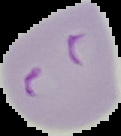

Summary:
  - Preparation: thin blood film
  - Image type: segmented cell region with the area outside set to black
  - Malaria status: parasitized
  - Image size: 121×136 pixels